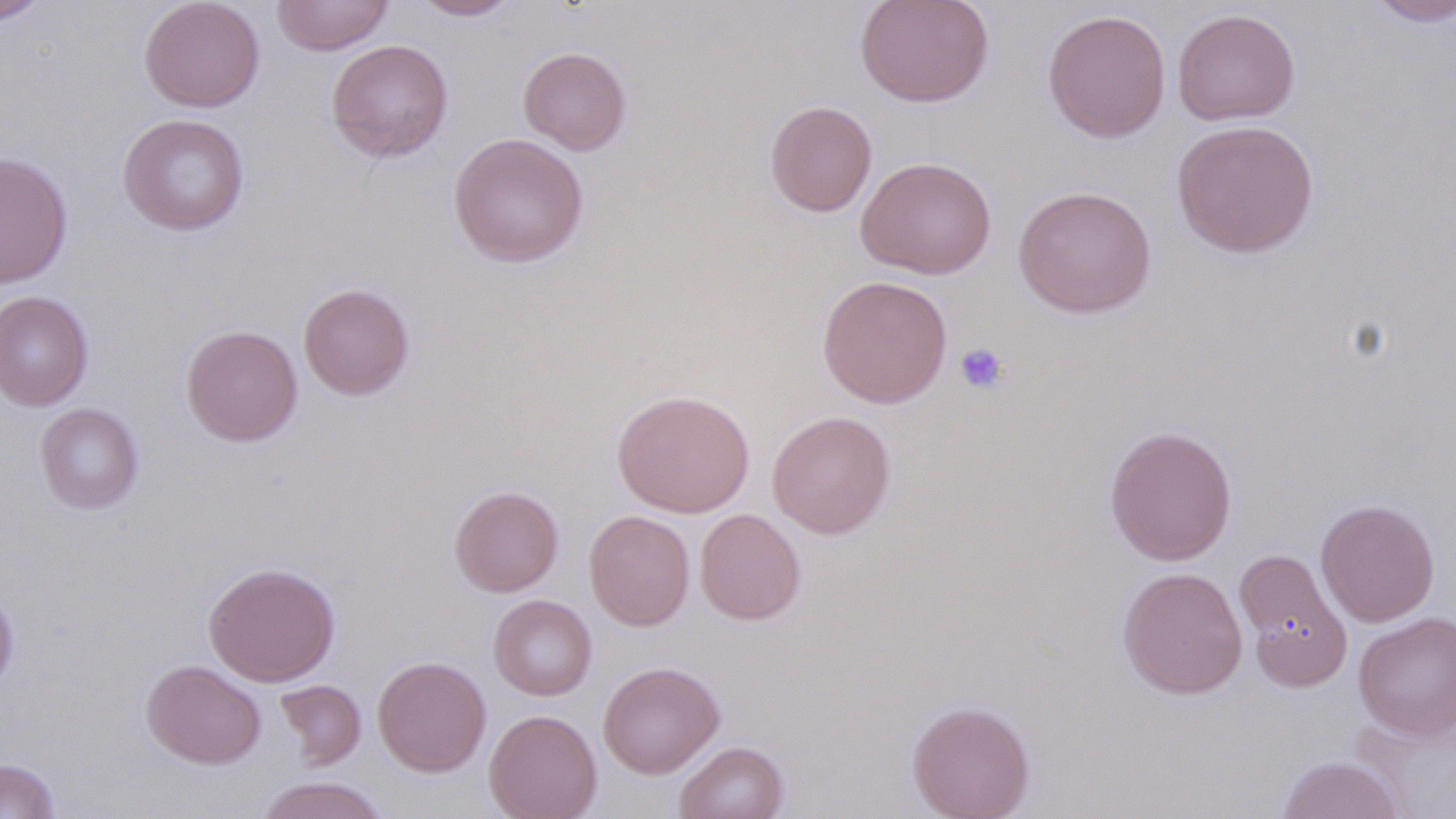

Approximate bounding boxes as named x1/y1/x2/y2 corners in pixels. Platelet locations: (x1=954, y1=342, x2=1009, y2=395). Uninfected red blood cell locations: (x1=0, y1=0, x2=52, y2=25), (x1=139, y1=0, x2=265, y2=112), (x1=271, y1=0, x2=394, y2=55), (x1=410, y1=0, x2=520, y2=21), (x1=854, y1=0, x2=994, y2=108), (x1=1364, y1=0, x2=1456, y2=27), (x1=1172, y1=8, x2=1300, y2=126), (x1=1042, y1=9, x2=1171, y2=143), (x1=326, y1=39, x2=453, y2=162), (x1=518, y1=47, x2=631, y2=155), (x1=764, y1=100, x2=877, y2=217), (x1=117, y1=113, x2=250, y2=236), (x1=1171, y1=119, x2=1319, y2=258), (x1=448, y1=133, x2=588, y2=268), (x1=0, y1=152, x2=73, y2=289), (x1=856, y1=156, x2=996, y2=279), (x1=1013, y1=186, x2=1156, y2=317), (x1=816, y1=275, x2=953, y2=408), (x1=298, y1=283, x2=415, y2=401), (x1=0, y1=290, x2=94, y2=411), (x1=181, y1=324, x2=303, y2=447), (x1=611, y1=389, x2=755, y2=517), (x1=35, y1=402, x2=145, y2=514), (x1=767, y1=410, x2=896, y2=538), (x1=1104, y1=424, x2=1237, y2=566), (x1=449, y1=485, x2=564, y2=597), (x1=1315, y1=499, x2=1440, y2=627), (x1=694, y1=508, x2=806, y2=625), (x1=584, y1=510, x2=695, y2=631), (x1=1234, y1=548, x2=1353, y2=690), (x1=203, y1=561, x2=341, y2=687), (x1=1117, y1=567, x2=1248, y2=699), (x1=0, y1=585, x2=20, y2=695), (x1=488, y1=595, x2=597, y2=700), (x1=1353, y1=612, x2=1456, y2=740), (x1=373, y1=656, x2=491, y2=777), (x1=141, y1=660, x2=266, y2=770), (x1=597, y1=661, x2=725, y2=779), (x1=274, y1=680, x2=366, y2=770), (x1=906, y1=699, x2=1035, y2=819), (x1=1352, y1=704, x2=1456, y2=818), (x1=483, y1=709, x2=602, y2=819), (x1=674, y1=740, x2=790, y2=819), (x1=1275, y1=755, x2=1406, y2=818), (x1=0, y1=758, x2=61, y2=819), (x1=253, y1=776, x2=392, y2=819). Slide-level diagnosis: no evidence of blood parasites. Single field of view. Image is 1456×819 pixels. 1000x magnification. Thin blood smear. May-Grünwald-Giemsa-stained preparation. Light microscopy.